State which parasite is depicted.
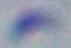
This is Toxoplasma gondii.

Photomicrograph. 1000x magnification.